Comment on the morphology of the erythrocytes.
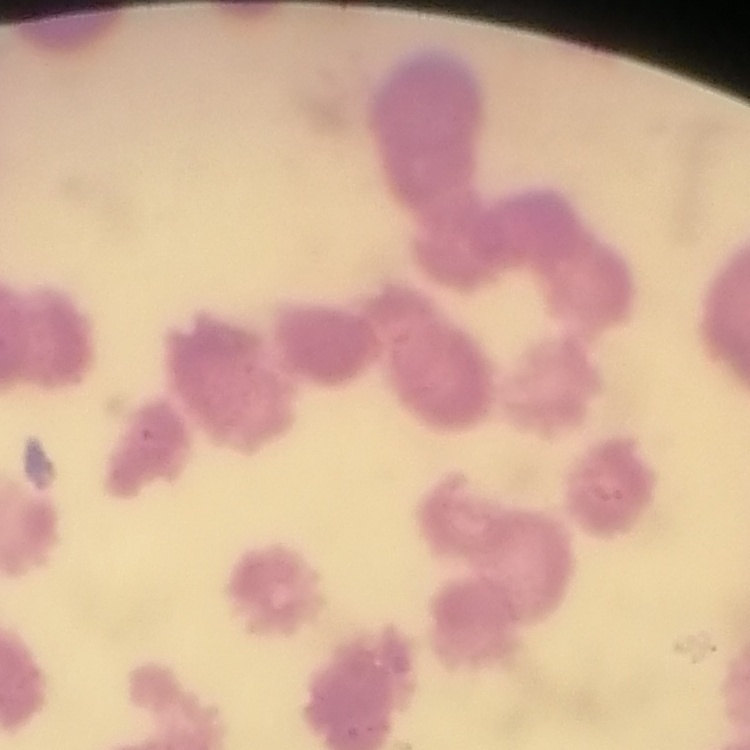

Rouleaux formation.

Summary:
  - Stain: Field's or Giemsa
  - Preparation: thin blood smear
  - Image type: square crop of a larger photomicrograph